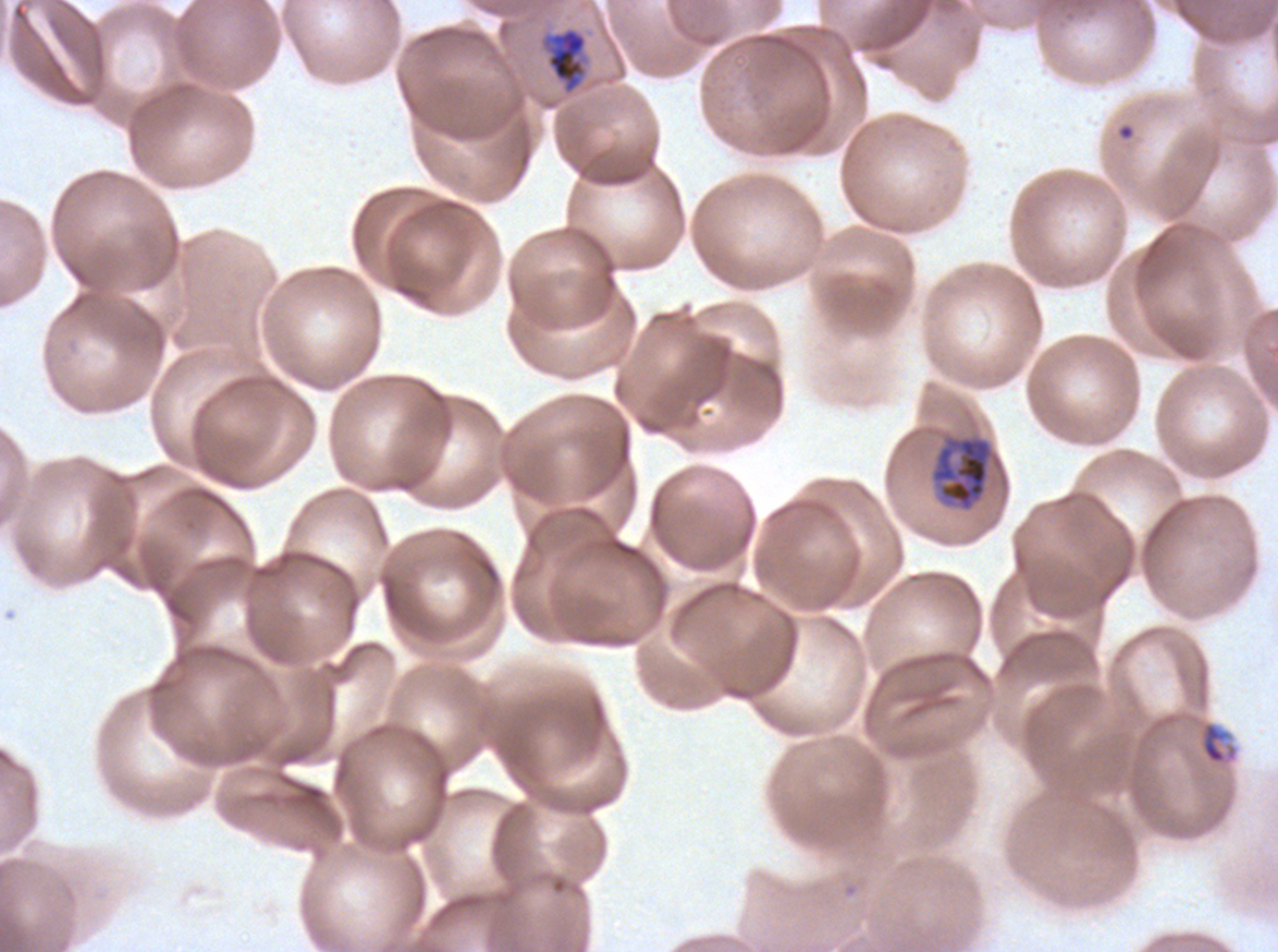
Approximate bounding rectangles given as corner coordinates in pixels from the top-left.
Summary:
  - Ring locations: (x1=1198, y1=720, x2=1239, y2=766)
  - Mid trophozoite locations: (x1=541, y1=27, x2=588, y2=94)
  - Late trophozoite locations: (x1=931, y1=436, x2=993, y2=511)
  - Field of view: one sub-image of a larger composite
  - Image size: 1278×952 pixels
  - Preparation: thin blood film
  - Life-cycle stages observed: ring, mid trophozoite, late trophozoite
  - Stain: Giemsa
  - Specimen: Plasmodium falciparum cultured ex vivo for 24 to 48 hours, from a patient in The Gambia